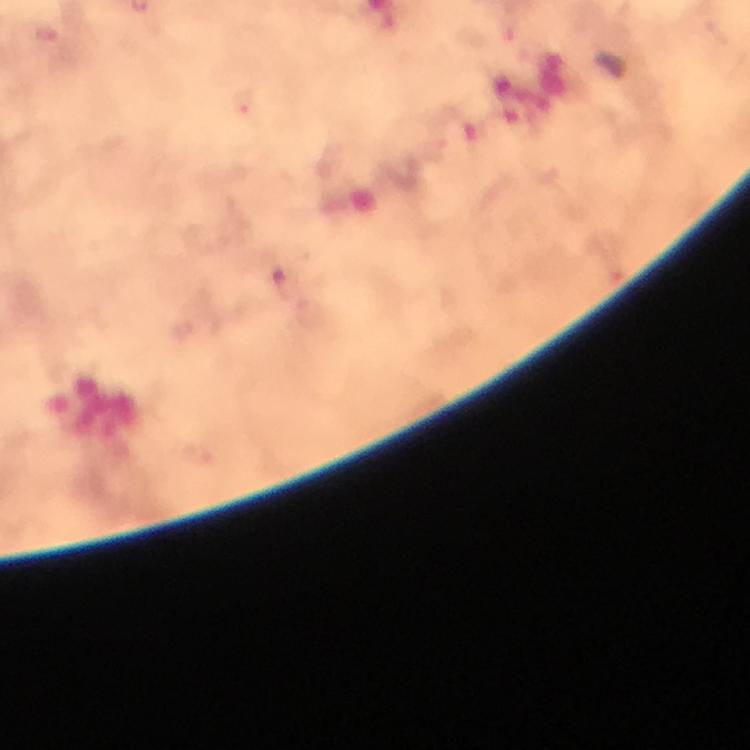

Approximate centers as (x, y) in pixels. Plasmodium parasite locations: (46, 33), (284, 283). From a diagnostic examination for malaria. 100x magnification. Photographed with a smartphone mounted on the microscope. Immersion oil was used. A crop from one field of view. Thick blood film. Image is 750×750 pixels. Giemsa-stained preparation.